Name the parasite shown.
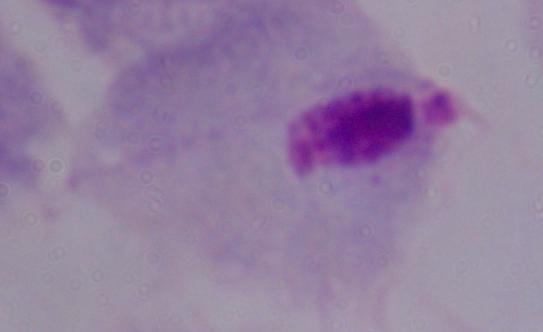

A trichomonad.

Captured at 1000x magnification. Photomicrograph.